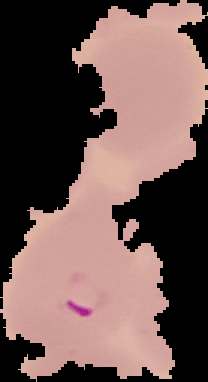
Summary:
  - Image type: segmented cell region on a black background
  - Malaria status: parasitized
  - Image size: 208×382 pixels
  - Preparation: thin blood film